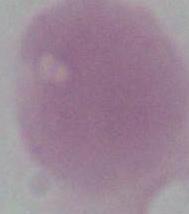

magnification = 1000x
identification = red blood cell
modality = micrograph